Assess this cell for malaria.
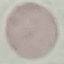

It is uninfected.

Acquired by smartphone through the microscope eyepiece. Giemsa stain. Thin smear of blood. Automatically extracted cell patch, resized to 64 × 64 pixels.